Assess this cell for malaria.
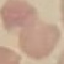
Uninfected.

Summary:
  - Capture: smartphone through the microscope eyepiece
  - Preparation: thin smear
  - Image type: automatically extracted cell patch, resized to 64 × 64 pixels
  - Stain: Giemsa